Name the blood parasite species.
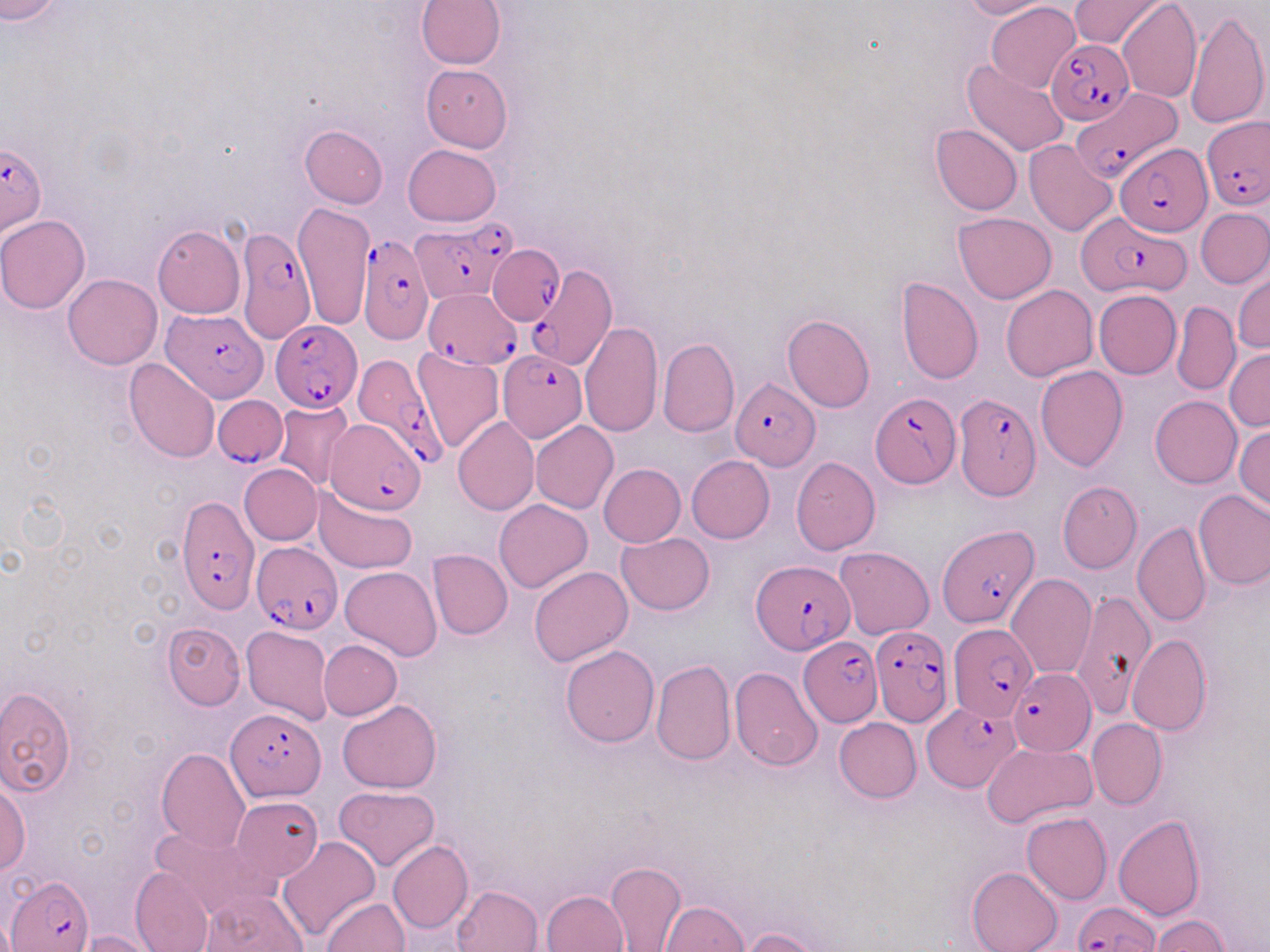

Plasmodium falciparum.

uninfected red blood cell locations = approximate bounding boxes as (x1,y1)-(x2,y2) corner pairs in pixels: (0,0)-(60,23), (416,0)-(506,70), (960,0)-(1057,19), (1069,0)-(1168,52), (1117,0)-(1202,101), (986,1)-(1081,92), (1185,8)-(1268,131), (961,59)-(1070,157), (420,64)-(513,152), (931,123)-(1023,216), (299,124)-(389,208), (1024,139)-(1117,236), (403,144)-(501,227), (294,202)-(375,330), (1196,209)-(1270,288), (953,212)-(1056,304), (0,215)-(90,313), (153,224)-(244,318), (1233,271)-(1269,354), (64,273)-(162,369), (895,277)-(983,386), (1001,285)-(1097,381), (1093,289)-(1181,379), (1169,302)-(1241,394), (781,313)-(874,412), (581,321)-(663,437), (657,337)-(739,438), (412,346)-(504,454), (1224,346)-(1270,431), (124,359)-(219,463), (1036,365)-(1128,471), (1149,395)-(1241,488), (271,401)-(356,492), (453,416)-(539,515), (531,421)-(619,513), (1234,423)-(1270,513), (686,456)-(775,543), (791,457)-(881,554), (598,463)-(685,547), (240,464)-(321,544), (1057,481)-(1141,574), (313,486)-(418,574), (1193,488)-(1270,591), (495,498)-(592,594), (1133,523)-(1211,628), (617,532)-(715,615), (834,546)-(934,640), (427,549)-(512,639), (529,565)-(633,665), (340,566)-(441,661), (1007,573)-(1097,679), (1071,592)-(1156,720), (162,624)-(245,709), (241,625)-(335,726), (1127,635)-(1211,736), (318,640)-(402,719), (561,644)-(660,747), (651,658)-(736,766), (730,667)-(823,771), (0,687)-(77,796), (337,700)-(442,793), (834,717)-(921,802), (1087,718)-(1167,809), (982,742)-(1096,827), (155,747)-(251,854), (0,779)-(29,875), (334,785)-(440,871), (229,795)-(324,882), (1021,811)-(1112,903), (1113,815)-(1206,921), (150,824)-(277,922), (276,836)-(380,944), (389,840)-(474,934), (604,860)-(686,952), (130,866)-(214,952), (967,866)-(1062,952), (453,885)-(543,952), (199,890)-(310,952), (542,890)-(629,952), (322,898)-(409,951), (659,900)-(749,952), (1149,914)-(1230,951), (740,927)-(826,952), (77,930)-(162,952)
stain = May-Grünwald-Giemsa
image size = 1270×952 pixels
preparation = thin blood smear
magnification = 1000x
modality = optical microscopy
Plasmodium falciparum-infected red blood cell locations = approximate bounding boxes as (x1,y1)-(x2,y2) corner pairs in pixels: (1046,40)-(1134,124), (1071,87)-(1182,183), (1204,116)-(1268,212), (0,142)-(48,237), (1116,142)-(1213,236), (1076,208)-(1185,299), (414,221)-(505,301), (236,226)-(316,346), (357,235)-(433,345), (490,243)-(561,320), (527,262)-(617,371), (424,288)-(520,367), (163,309)-(266,402), (272,320)-(359,411), (497,348)-(586,443), (349,359)-(445,472), (730,377)-(820,472), (871,392)-(960,488), (955,393)-(1041,500), (217,394)-(289,469), (325,420)-(428,515), (175,497)-(258,615), (937,524)-(1039,628), (250,539)-(342,633), (752,559)-(855,655), (947,625)-(1035,723), (870,627)-(951,726), (798,637)-(883,726), (1009,668)-(1096,755), (923,701)-(1021,792), (226,707)-(326,801), (6,874)-(93,951), (1072,901)-(1158,951)
field of view = single